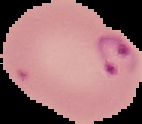
preparation = thin blood smear
image type = cell region segmented out of the field of view; surrounding area masked to black
result = Plasmodium parasites detected
image size = 142×124 pixels